Give the extent of all Plasmodium vivax-infected red blood cells.
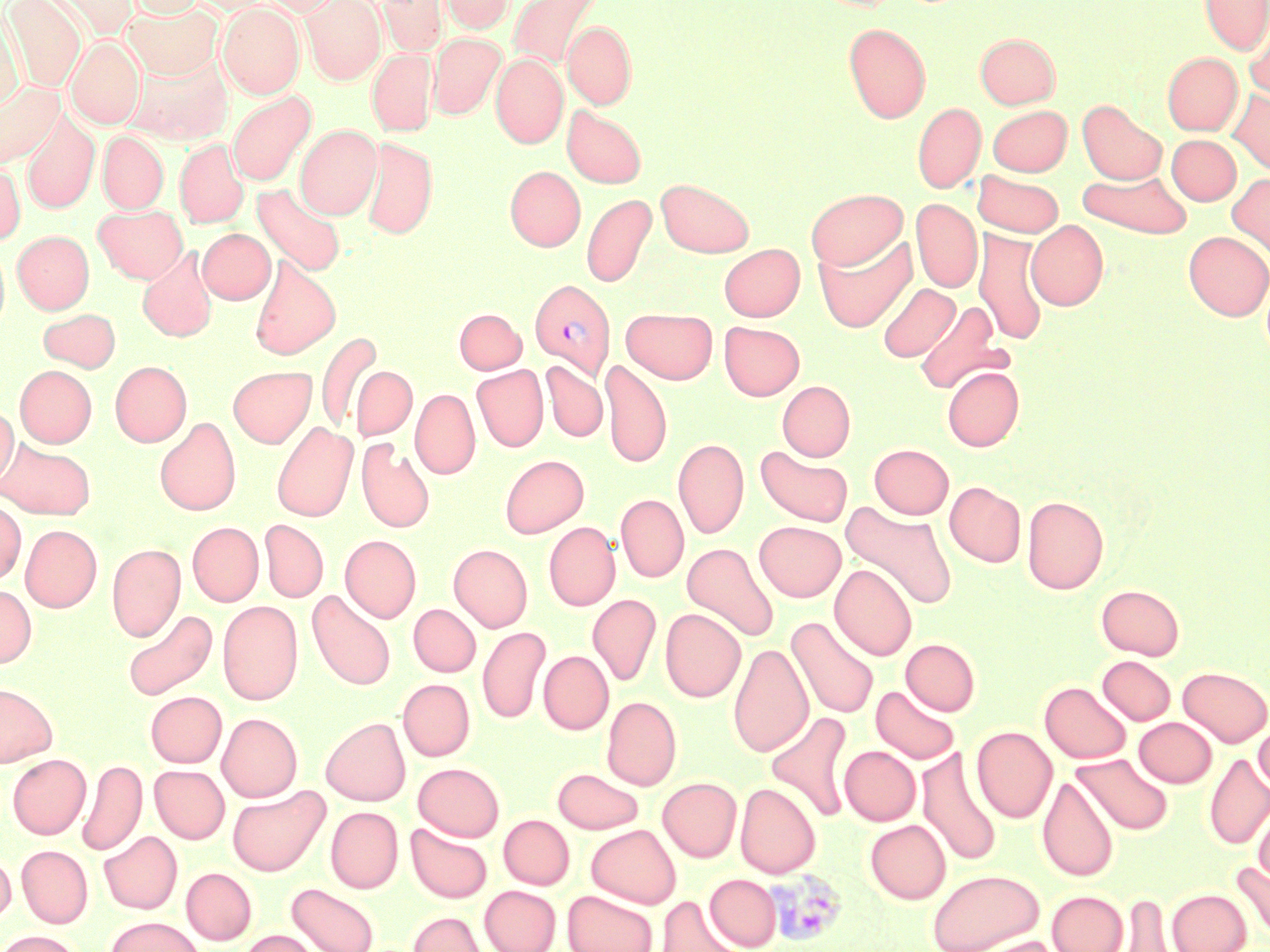

Approximate bounding boxes as (x1, y1, x2, y2) in pixels.
Plasmodium vivax-infected red blood cells: (530, 279, 615, 378), (764, 868, 847, 948).

Summary:
  - Uninfected red blood cell locations: (3, 0, 87, 93), (45, 0, 137, 40), (124, 0, 207, 18), (258, 0, 343, 17), (301, 0, 386, 84), (377, 0, 447, 56), (438, 0, 515, 34), (508, 0, 605, 72), (1200, 0, 1270, 55), (217, 3, 305, 98), (122, 4, 223, 80), (0, 8, 26, 114), (1244, 12, 1270, 99), (563, 20, 636, 109), (844, 23, 930, 124), (428, 33, 505, 120), (976, 33, 1059, 108), (66, 38, 144, 129), (368, 49, 437, 136), (125, 51, 233, 146), (1162, 52, 1242, 135), (491, 54, 567, 148), (0, 82, 64, 169), (1227, 88, 1270, 175), (227, 89, 316, 187), (912, 101, 986, 193), (1077, 101, 1167, 185), (987, 105, 1072, 176), (562, 106, 646, 187), (21, 109, 100, 215), (295, 124, 382, 219), (98, 131, 168, 213), (1166, 134, 1241, 205), (360, 137, 437, 239), (175, 138, 249, 229), (0, 161, 25, 245), (505, 166, 585, 251), (1078, 167, 1192, 238), (972, 170, 1064, 237), (1227, 172, 1270, 259), (656, 178, 755, 258), (253, 183, 346, 277), (805, 188, 907, 270), (581, 193, 656, 287), (911, 198, 983, 293), (94, 204, 187, 283), (1026, 220, 1108, 310), (198, 229, 275, 304), (974, 229, 1048, 346), (13, 230, 94, 313), (1183, 230, 1270, 321), (813, 234, 917, 333), (719, 243, 805, 321), (0, 244, 9, 333), (138, 246, 219, 342), (249, 256, 341, 360), (877, 282, 959, 362), (915, 300, 1009, 395), (38, 308, 121, 373), (455, 308, 526, 374), (622, 308, 718, 384), (719, 321, 804, 400), (316, 330, 382, 434), (600, 358, 672, 468), (110, 361, 192, 446), (540, 361, 607, 442), (472, 364, 548, 452), (15, 365, 97, 447), (228, 366, 317, 448), (351, 366, 417, 440), (942, 366, 1023, 451), (778, 380, 855, 461), (410, 388, 480, 479), (0, 405, 18, 488), (155, 417, 241, 515), (272, 421, 358, 522), (356, 437, 435, 533), (1, 438, 96, 519), (673, 438, 748, 539), (869, 443, 954, 519), (756, 446, 853, 527), (500, 454, 588, 538), (945, 481, 1026, 567), (616, 494, 689, 582), (1022, 496, 1108, 594), (0, 500, 26, 585), (841, 501, 958, 611), (259, 519, 329, 602), (754, 521, 846, 602), (187, 522, 263, 606), (544, 522, 620, 611), (20, 524, 102, 612), (340, 534, 421, 623), (682, 541, 779, 642), (106, 543, 185, 641), (449, 544, 532, 631), (830, 563, 917, 661), (0, 584, 37, 668), (1097, 584, 1184, 659), (306, 589, 396, 691), (587, 593, 661, 686), (217, 601, 303, 705), (408, 603, 481, 677), (121, 608, 219, 701), (660, 608, 746, 702), (786, 616, 879, 719), (478, 625, 551, 725), (901, 639, 980, 716), (728, 642, 813, 757), (539, 650, 613, 734), (1098, 655, 1176, 725), (1178, 666, 1270, 747), (398, 678, 475, 761), (1040, 681, 1131, 763), (0, 682, 58, 767), (870, 685, 960, 765), (146, 691, 226, 767), (601, 695, 681, 790), (765, 711, 855, 822), (217, 713, 302, 802), (321, 717, 410, 805), (1134, 717, 1217, 787), (1254, 720, 1270, 792), (971, 726, 1057, 823), (840, 745, 921, 825), (917, 747, 1003, 867), (1072, 753, 1174, 835), (1204, 753, 1270, 849), (8, 754, 91, 839), (77, 759, 147, 856), (413, 762, 504, 841), (149, 765, 229, 843), (552, 768, 644, 834), (1037, 774, 1119, 882), (658, 777, 742, 862), (735, 782, 821, 878), (227, 785, 329, 876), (1253, 804, 1270, 884), (325, 806, 403, 893), (499, 815, 574, 889), (865, 819, 951, 904), (405, 823, 492, 903), (586, 824, 681, 908), (99, 831, 182, 913), (16, 845, 93, 928), (0, 850, 15, 924), (1231, 860, 1270, 943), (181, 868, 256, 944), (927, 868, 1044, 952), (705, 873, 781, 950), (286, 883, 379, 952), (479, 885, 560, 952), (1167, 888, 1251, 952), (562, 890, 658, 952), (1047, 890, 1128, 952), (1112, 892, 1180, 951), (656, 895, 746, 952), (407, 911, 488, 952), (105, 916, 205, 952), (0, 930, 83, 952), (238, 930, 322, 952), (964, 936, 1065, 952)
  - Slide-level diagnosis: Plasmodium vivax
  - Preparation: thin blood film
  - Stain: May-Grünwald-Giemsa
  - Field of view: one of a larger specimen
  - Image size: 1270×952 pixels
  - Modality: light microscopy
  - Magnification: 1000x